State which parasite is depicted.
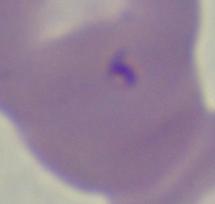

This is Babesia.

Summary:
  - Magnification: 1000x
  - Modality: micrograph